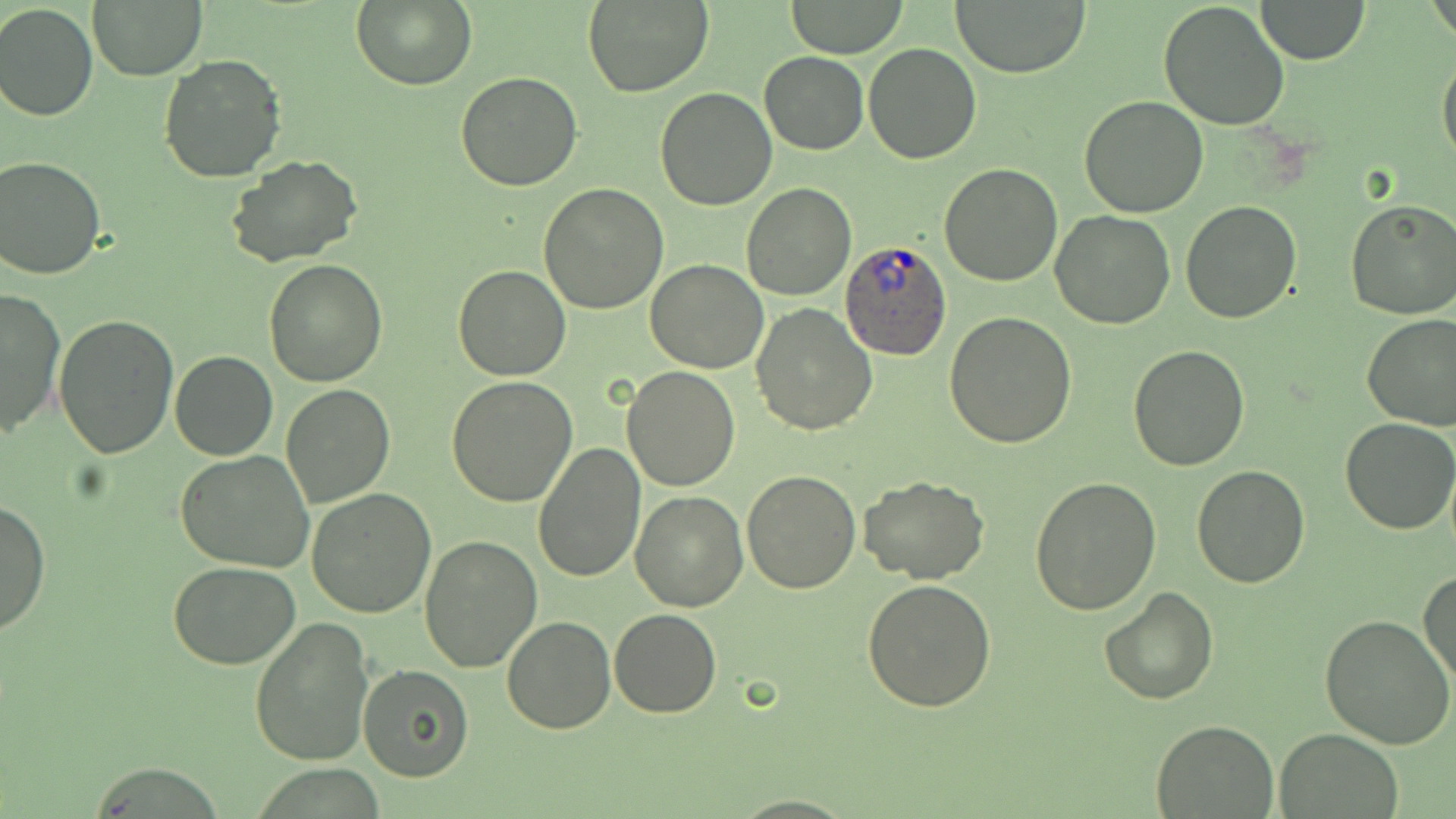

Approximate bounding boxes as [x1, y1, x2, y2] in pixels. Uninfected red blood cell locations: [87, 0, 210, 81], [351, 0, 476, 91], [783, 0, 910, 58], [948, 0, 1094, 76], [1256, 0, 1370, 64], [580, 1, 714, 99], [1157, 2, 1289, 132], [0, 3, 98, 121], [862, 43, 982, 164], [1438, 45, 1456, 170], [759, 52, 869, 155], [157, 54, 287, 184], [456, 70, 583, 191], [655, 86, 778, 211], [1079, 95, 1208, 218], [226, 154, 363, 267], [0, 156, 106, 280], [939, 165, 1062, 286], [741, 182, 856, 301], [538, 183, 668, 314], [1180, 200, 1303, 324], [1345, 200, 1456, 320], [1051, 209, 1178, 330], [263, 258, 388, 388], [646, 259, 767, 374], [455, 264, 571, 380], [1, 287, 66, 436], [750, 302, 877, 434], [944, 312, 1079, 448], [54, 313, 179, 458], [1361, 314, 1456, 431], [1127, 345, 1250, 470], [170, 350, 278, 460], [621, 366, 740, 491], [446, 376, 578, 506], [282, 384, 394, 507], [1341, 418, 1455, 534], [533, 443, 646, 583], [176, 449, 315, 573], [1192, 464, 1309, 587], [740, 469, 862, 594], [858, 475, 988, 585], [1030, 477, 1162, 614], [307, 486, 437, 618], [627, 491, 748, 612], [1, 498, 49, 635], [420, 535, 543, 671], [170, 561, 299, 669], [1419, 570, 1456, 690], [862, 579, 997, 713], [1098, 586, 1219, 703], [608, 608, 721, 717], [1321, 613, 1455, 750], [502, 615, 616, 734], [250, 617, 375, 767], [358, 664, 472, 782], [1150, 719, 1277, 817], [1274, 730, 1404, 819]. Plasmodium ovale-infected red blood cell locations: [841, 236, 953, 360]. Slide-level diagnosis: Plasmodium ovale. May-Grünwald-Giemsa-stained preparation. 1000x magnification. Optical microscopy. Image is 1456×819 pixels. Thin blood film. Single field of view.